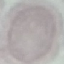
Summary:
  - Malaria status: uninfected
  - Image type: cell patch, automatically extracted from a larger field of view and resized to 64 × 64 pixels
  - Preparation: thin smear
  - Capture: smartphone camera at the microscope eyepiece
  - Stain: Giemsa